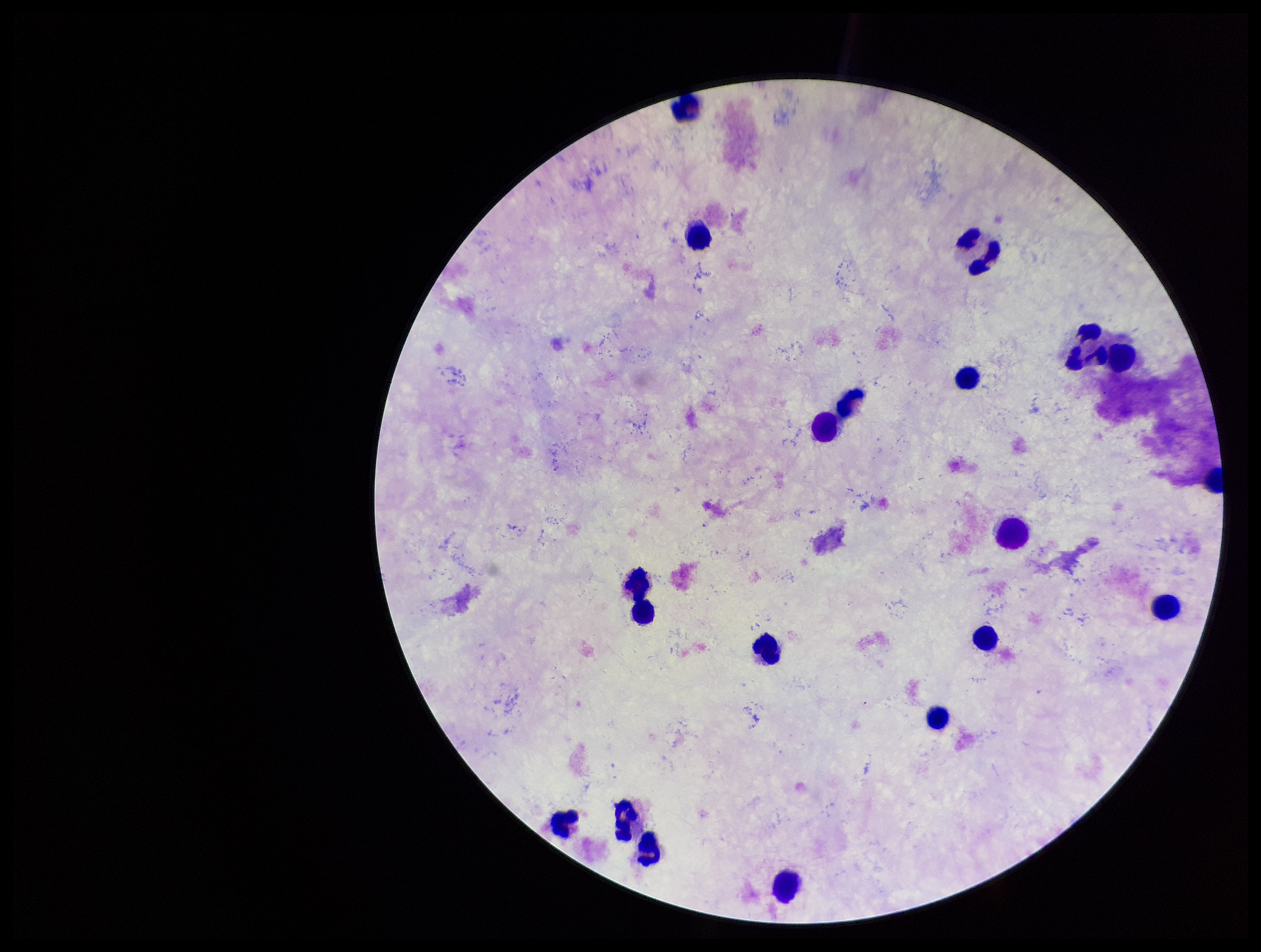

Summary:
  - Patient malaria status: negative
  - Capture: smartphone photograph through the microscope eyepiece
  - Plasmodium parasites: none detected
  - Image size: 1261×952 pixels
  - Stain: Giemsa
  - Preparation: thick blood smear
  - Leukocyte count: 17
  - Parasite count: 0
  - Field of view: single